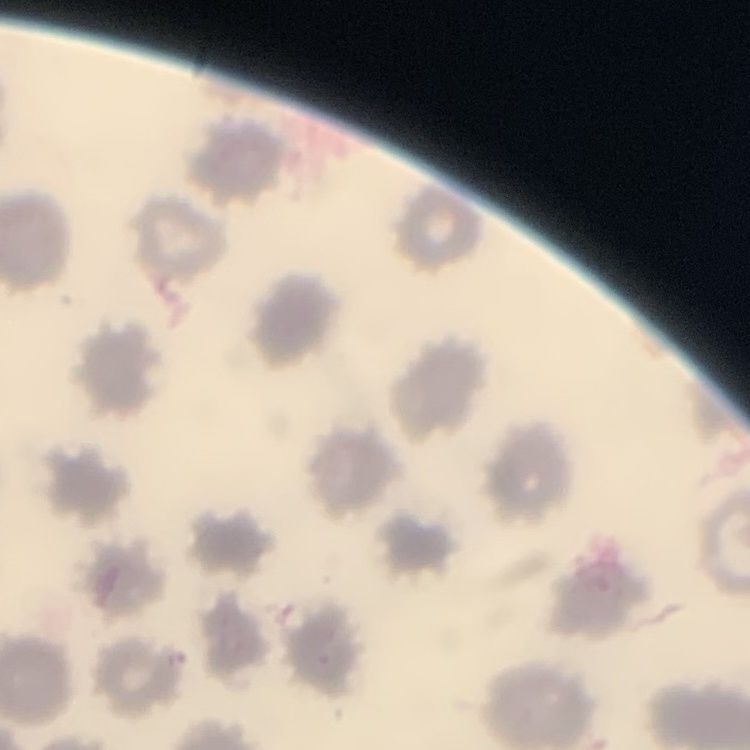
The red blood cells show no rouleaux formation. Square crop of a larger photomicrograph. Thin peripheral smear. Field's or Giemsa stain.